Point out each leukocyte.
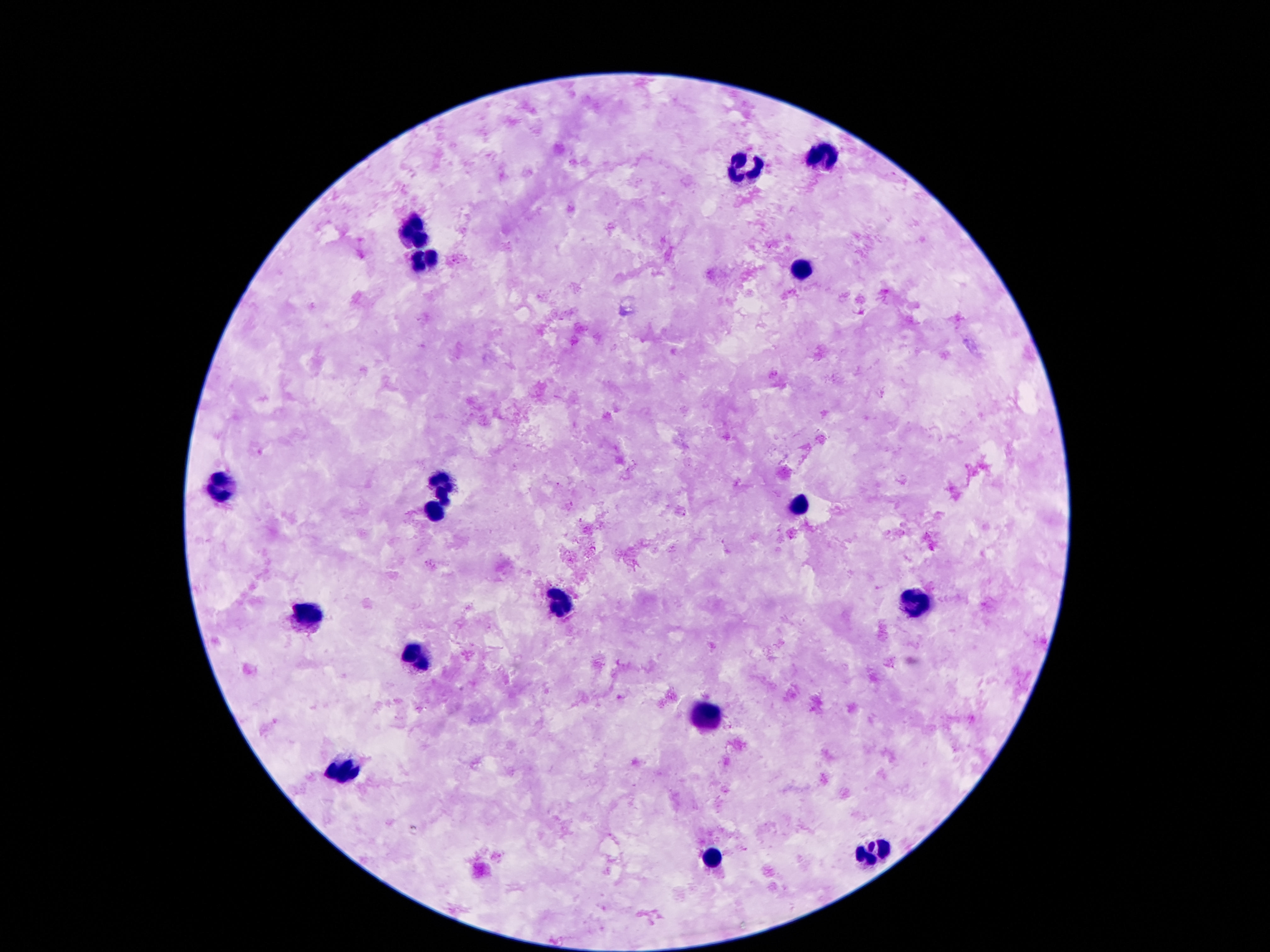

Approximate object centers, in pixels from the top-left corner.
Leukocytes: (x=824, y=157), (x=747, y=168), (x=415, y=232), (x=426, y=259), (x=801, y=266), (x=445, y=482), (x=215, y=486), (x=797, y=503), (x=434, y=512), (x=912, y=601), (x=560, y=604), (x=304, y=612), (x=418, y=656), (x=712, y=717), (x=343, y=767), (x=874, y=853), (x=713, y=858).

Summary:
  - Stain: Giemsa
  - Preparation: thick peripheral-blood smear
  - Image size: 1270×952 pixels
  - Capture: smartphone camera through the microscope eyepiece
  - Magnification: 100x
  - Patient malaria status: uninfected
  - Field of view: single